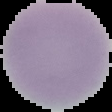
image type = segmented cell region with the area outside set to black
image size = 112×112 pixels
result = no malaria parasites detected
preparation = thin blood smear